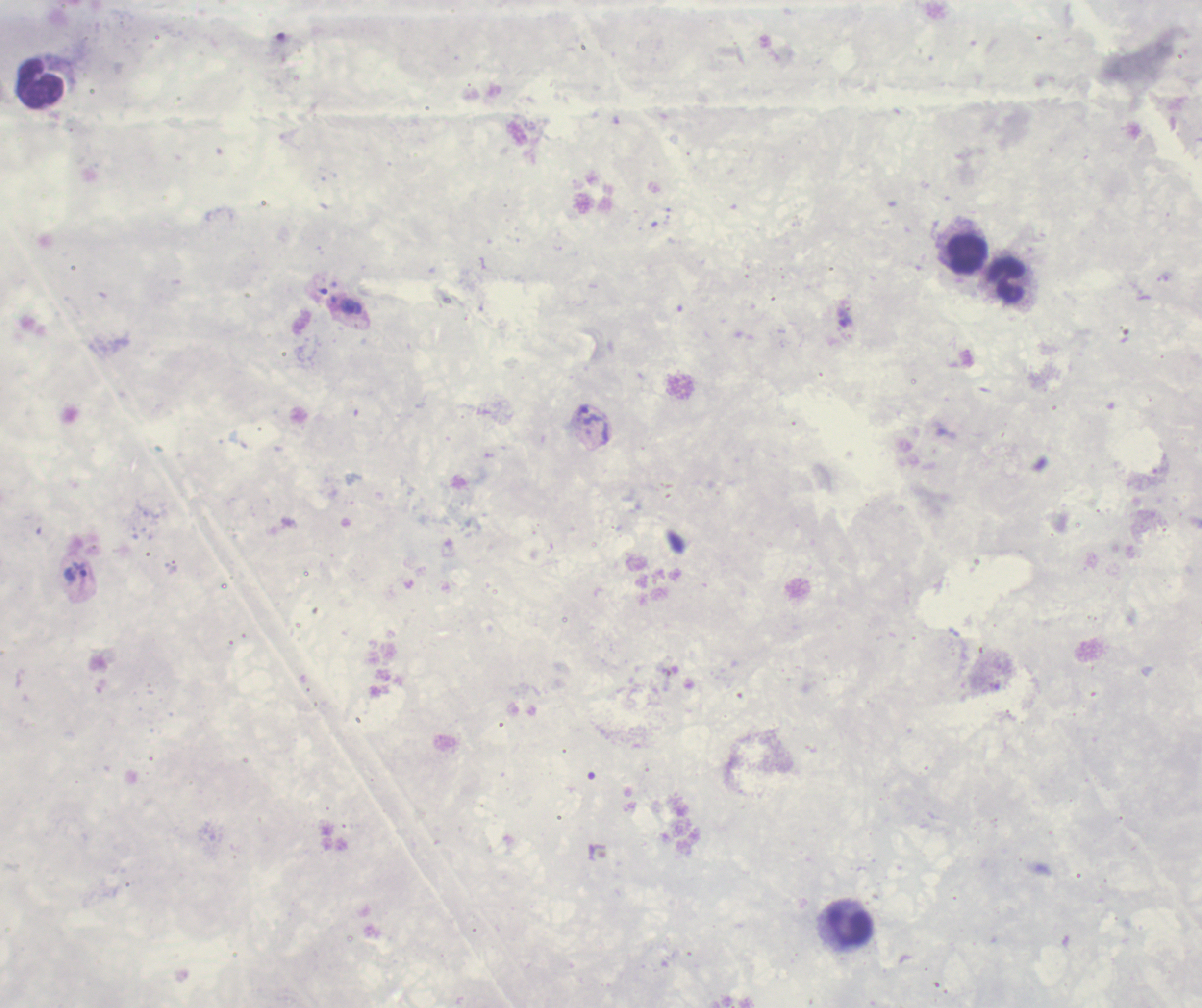
Approximate object centers, in pixels from the top-left corner. Trophozoite locations: (x=353, y=308), (x=589, y=416), (x=77, y=572). Leukocyte locations: (x=41, y=83), (x=966, y=254), (x=1006, y=280), (x=849, y=925). Romanowsky-stained preparation. 100x magnification. Result: malaria parasites detected. Background quality: poor. Thick blood film. Previously used in a real diagnosis. Single field of view. Image is 1202×1008 pixels.